Classify this cell by malaria status.
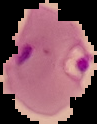

It is parasitized.

image size = 97×124 pixels
image type = cell region segmented out of the field of view; surrounding area masked to black
preparation = thin blood film